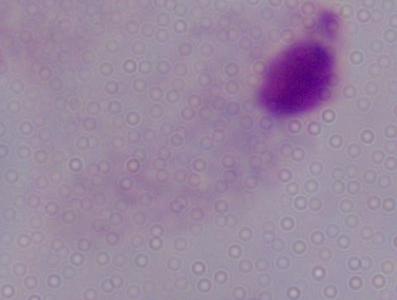
{
  "identification": "trichomonad",
  "modality": "photomicrograph",
  "magnification": "1000x"
}